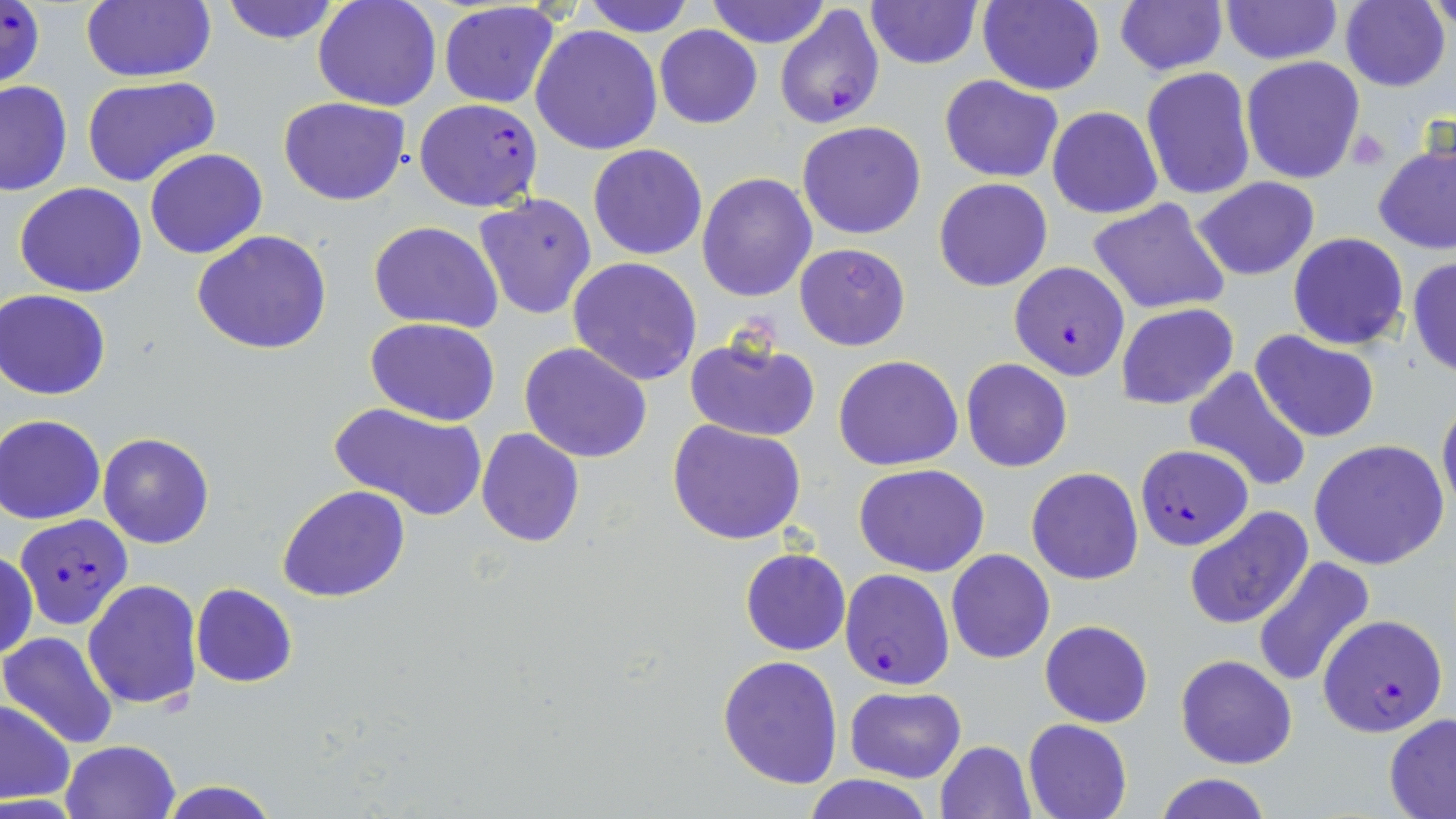
Summary:
  - Coordinate format: approximate bounding boxes as [x1, y1, x2, y2] in pixels
  - Plasmodium falciparum-infected red blood cell locations: [0, 0, 47, 90], [773, 5, 885, 130], [412, 98, 544, 212], [1010, 262, 1129, 381], [1134, 446, 1250, 550], [14, 514, 134, 634], [840, 567, 956, 691], [1319, 613, 1449, 735]
  - Platelet locations: [1349, 128, 1393, 171]
  - Uninfected red blood cell locations: [81, 0, 217, 84], [312, 0, 442, 111], [580, 0, 693, 37], [705, 0, 831, 49], [1219, 0, 1342, 67], [1340, 0, 1450, 92], [1426, 0, 1454, 36], [218, 1, 343, 46], [865, 1, 982, 70], [977, 1, 1105, 95], [437, 2, 560, 109], [1115, 2, 1227, 75], [530, 24, 662, 155], [653, 25, 763, 129], [1241, 55, 1367, 185], [1141, 68, 1256, 200], [80, 74, 220, 187], [940, 74, 1064, 181], [0, 80, 72, 196], [278, 97, 410, 206], [1045, 105, 1163, 219], [796, 121, 927, 240], [1373, 139, 1456, 255], [588, 144, 707, 260], [144, 147, 268, 259], [697, 171, 819, 302], [933, 176, 1053, 291], [1191, 176, 1320, 280], [14, 182, 148, 298], [474, 194, 598, 321], [1086, 198, 1232, 315], [369, 221, 503, 331], [191, 230, 334, 355], [1288, 232, 1409, 350], [794, 243, 910, 350], [1408, 255, 1456, 378], [567, 256, 703, 386], [2, 289, 114, 399], [1115, 304, 1238, 410], [365, 317, 499, 423], [1251, 330, 1382, 442], [683, 333, 821, 443], [520, 342, 653, 464], [833, 355, 963, 471], [961, 357, 1073, 472], [1184, 368, 1311, 495], [1437, 396, 1456, 520], [329, 400, 487, 520], [1, 415, 105, 524], [666, 420, 808, 545], [475, 428, 587, 546], [97, 432, 214, 548], [1310, 439, 1450, 571], [853, 463, 989, 576], [1027, 466, 1145, 585], [278, 486, 410, 604], [1184, 505, 1314, 629], [740, 548, 850, 656], [946, 548, 1055, 665], [1, 549, 37, 661], [1252, 555, 1377, 689], [83, 579, 203, 710], [190, 582, 298, 687], [1040, 620, 1153, 728], [2, 632, 121, 748], [717, 654, 843, 790], [1174, 654, 1297, 769], [844, 686, 966, 782], [0, 701, 75, 804], [1384, 713, 1456, 816], [1023, 718, 1132, 819], [59, 740, 182, 819], [934, 741, 1037, 819], [1155, 773, 1272, 819], [800, 775, 932, 819], [156, 780, 281, 819]
  - Slide-level diagnosis: Plasmodium falciparum
  - Magnification: 1000x
  - Image size: 1456×819 pixels
  - Modality: light microscopy
  - Preparation: thin blood smear
  - Field of view: one of a larger specimen
  - Stain: May-Grünwald-Giemsa